Comment on the morphology of the erythrocytes.
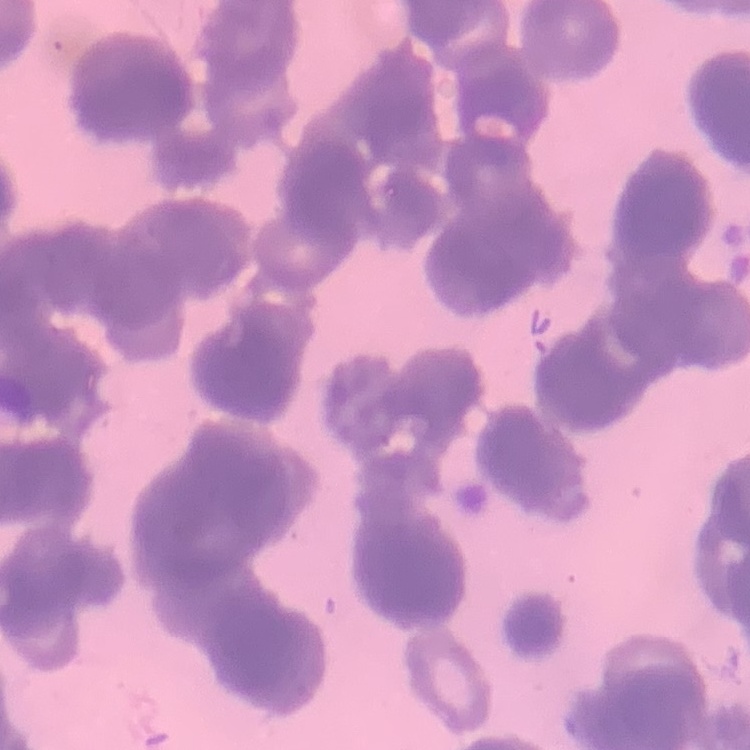

They show rouleaux formation.

Summary:
  - Image type: one tile cut from a larger photomicrograph
  - Preparation: thin peripheral smear
  - Stain: Field's or Giemsa